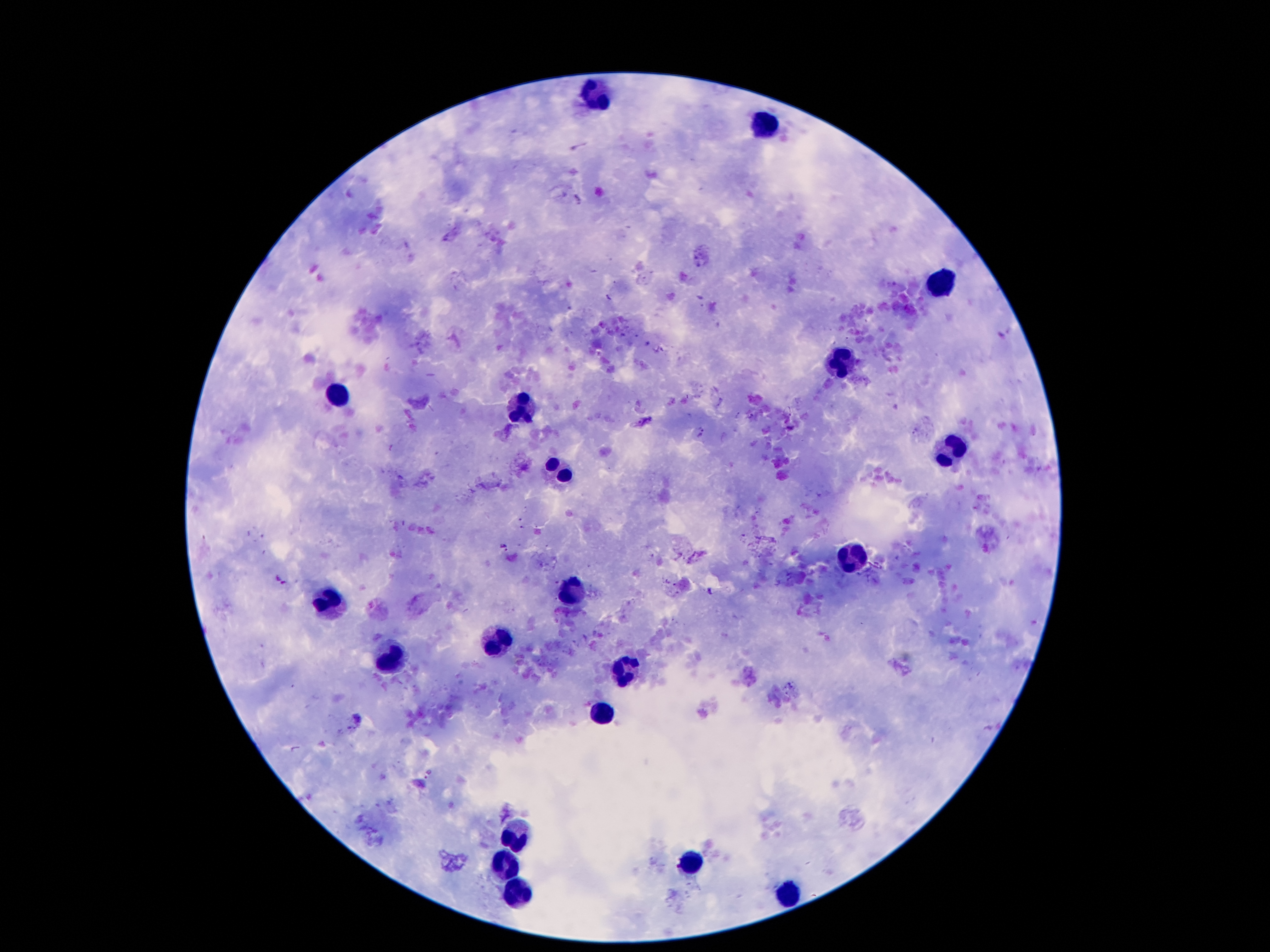 Approximate centers as [x, y] in pixels. Leukocyte locations: [596, 97], [764, 124], [939, 283], [841, 360], [339, 392], [521, 408], [948, 449], [557, 469], [852, 555], [575, 592], [325, 596], [500, 642], [387, 658], [628, 669], [600, 712], [509, 830], [693, 862], [507, 864], [516, 891], [784, 891]. Malaria parasite locations: [788, 411], [738, 415], [915, 432], [701, 434], [502, 546], [427, 774]. Image is 1270×952 pixels. Patient malaria status: infected with Plasmodium falciparum. Giemsa-stained preparation. Thick blood smear. Photographed through the microscope eyepiece with a smartphone camera. Single field of view. 100x magnification.